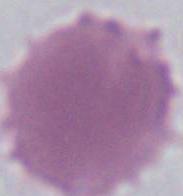
modality = photomicrograph
identification = erythrocyte
magnification = 1000x